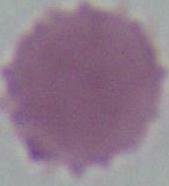

Summary:
  - Magnification: 1000x
  - Identification: red blood cell
  - Modality: photomicrograph